Assess this cell for malaria.
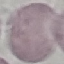

Uninfected.

image type = cell patch, automatically extracted from a larger field of view and resized to 64 × 64 pixels
preparation = thin smear
capture = smartphone camera at the microscope eyepiece
stain = Giemsa